Name the parasite shown.
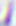
This is Toxoplasma gondii.

magnification: 400x
modality: photomicrograph